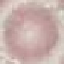

Malaria status: uninfected. Thin blood film. Cell patch, automatically extracted from a larger field of view and resized to 64 × 64 pixels. Giemsa stain. Photographed with a smartphone camera at the microscope eyepiece.